Classify this cell by malaria status.
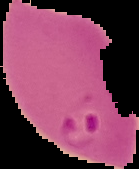
Parasitized.

preparation: thin blood film
image_type: segmented cell region with the area outside set to black
image_size: 139×169 pixels